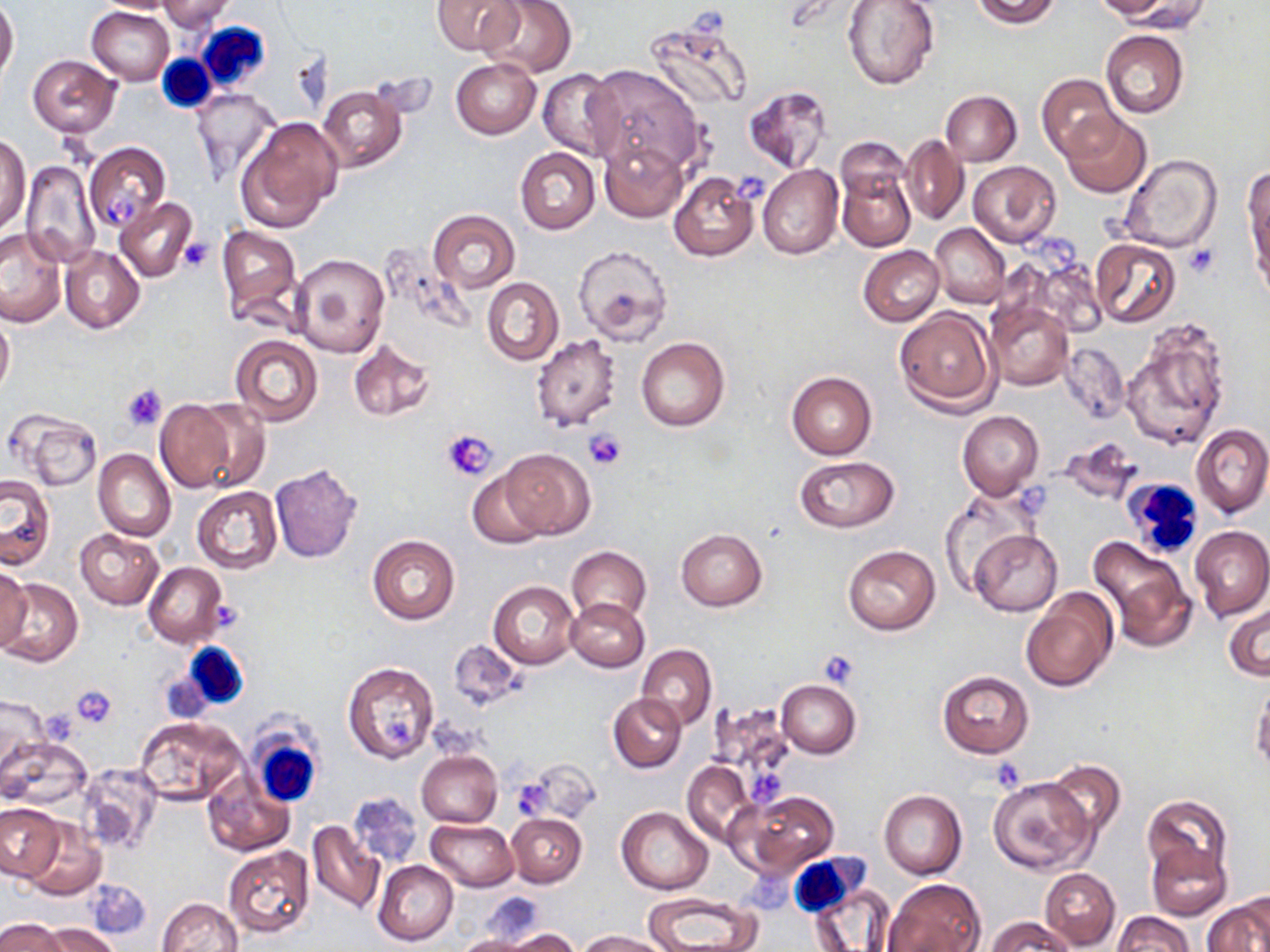

Approximate bounding boxes as (x1,y1)-(x2,y2) corner pairs in pixels. Platelet locations: (733,172)-(772,205), (100,194)-(139,224), (1042,235)-(1076,276), (178,237)-(213,272), (1184,245)-(1220,279), (122,383)-(169,430), (442,428)-(499,480), (583,428)-(626,469), (819,649)-(860,689), (71,684)-(117,729), (381,719)-(418,748), (988,757)-(1026,791), (749,768)-(784,805), (518,782)-(549,818), (747,865)-(794,917). Uninfected red blood cell locations: (92,0)-(183,14), (432,0)-(522,57), (478,0)-(576,78), (843,0)-(940,89), (969,0)-(1064,29), (1092,0)-(1181,21), (157,1)-(236,31), (1111,1)-(1208,31), (0,2)-(18,79), (87,5)-(175,84), (644,16)-(754,113), (1101,30)-(1189,119), (27,54)-(121,138), (451,58)-(541,138), (583,63)-(706,177), (538,68)-(620,160), (1038,73)-(1121,161), (318,84)-(409,171), (743,86)-(833,173), (191,88)-(279,186), (941,91)-(1021,166), (1061,112)-(1153,198), (237,119)-(342,229), (1,133)-(30,233), (901,134)-(969,225), (837,137)-(910,203), (599,139)-(688,222), (85,142)-(170,233), (515,147)-(601,233), (1118,153)-(1221,254), (21,159)-(101,268), (969,161)-(1060,247), (757,164)-(843,259), (836,168)-(915,250), (1245,171)-(1270,283), (669,172)-(759,262), (116,197)-(198,282), (427,209)-(521,293), (931,223)-(1010,309), (217,225)-(302,329), (1,229)-(66,326), (1089,240)-(1181,327), (573,245)-(673,346), (858,245)-(944,325), (59,246)-(144,334), (290,253)-(389,358), (482,277)-(563,366), (985,303)-(1073,390), (895,307)-(999,413), (0,313)-(14,398), (1122,320)-(1232,451), (230,334)-(322,426), (531,334)-(622,431), (636,336)-(730,431), (347,338)-(436,421), (1059,342)-(1130,425), (786,370)-(876,460), (155,399)-(235,493), (189,400)-(271,492), (957,411)-(1044,501), (12,412)-(104,491), (1192,424)-(1270,518), (1057,439)-(1143,506), (500,449)-(596,538), (94,450)-(176,542), (793,454)-(900,533), (269,463)-(363,563), (466,470)-(547,548), (0,475)-(55,570), (192,487)-(282,573), (939,492)-(1036,592), (75,528)-(163,609), (676,528)-(767,609), (1190,528)-(1270,621), (968,529)-(1061,616), (368,534)-(459,625), (1087,534)-(1197,652), (842,545)-(939,635), (567,546)-(651,626), (145,563)-(226,647), (0,564)-(32,654), (0,576)-(83,667), (488,581)-(579,668), (1022,588)-(1119,693), (566,597)-(649,672), (1224,602)-(1269,681), (449,639)-(525,713), (637,643)-(717,729), (343,662)-(438,763), (938,670)-(1033,756), (776,680)-(861,758), (1250,680)-(1270,772), (608,693)-(686,772), (0,695)-(52,788), (707,703)-(796,784), (134,717)-(247,806), (3,738)-(89,809), (417,750)-(503,828), (1044,758)-(1127,841), (682,760)-(757,846), (76,762)-(160,855), (203,774)-(295,856), (987,777)-(1095,876), (737,790)-(840,878), (879,790)-(966,879), (348,791)-(422,868), (1143,796)-(1232,881), (0,803)-(63,881), (617,808)-(713,894), (506,813)-(586,887), (426,819)-(518,891), (307,821)-(384,916), (21,822)-(106,899), (1145,843)-(1230,920), (223,844)-(315,937), (373,860)-(459,946), (1039,867)-(1120,949), (885,878)-(983,952), (84,879)-(149,939), (805,881)-(897,952), (642,892)-(765,952), (1204,895)-(1268,952), (156,898)-(242,952), (473,898)-(554,944), (1111,912)-(1193,952), (986,916)-(1076,952), (1,918)-(66,952), (41,923)-(121,952), (503,929)-(580,952), (578,930)-(672,951), (456,933)-(542,952). White blood cell locations: (197,19)-(272,92), (158,56)-(215,113), (1122,480)-(1197,563), (179,643)-(249,711), (247,720)-(322,808), (789,856)-(881,937). Slide-level diagnosis: negative for blood parasites. May-Grünwald-Giemsa-stained preparation. Image is 1270×952 pixels. Single field of view. Captured at 1000x magnification. Thin blood film. Optical microscopy.